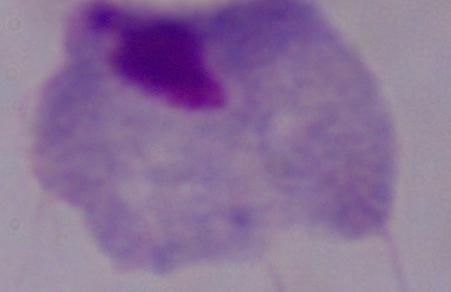

Summary:
  - Modality: micrograph
  - Magnification: 1000x
  - Identification: trichomonad